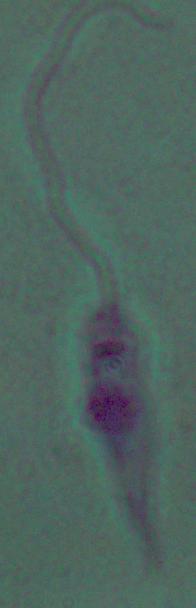
Summary:
  - Magnification: 1000x
  - Modality: micrograph
  - Identification: Leishmania